Assess this cell for malaria.
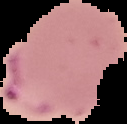

It is parasitized.

image_size: 127×124 pixels
preparation: thin blood smear
image_type: segmented cell region on a black background